Classify this cell by malaria status.
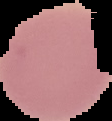
It is uninfected.

Segmented cell region on a black background. Image is 112×121 pixels. From a thin blood smear.